Find each white blood cell.
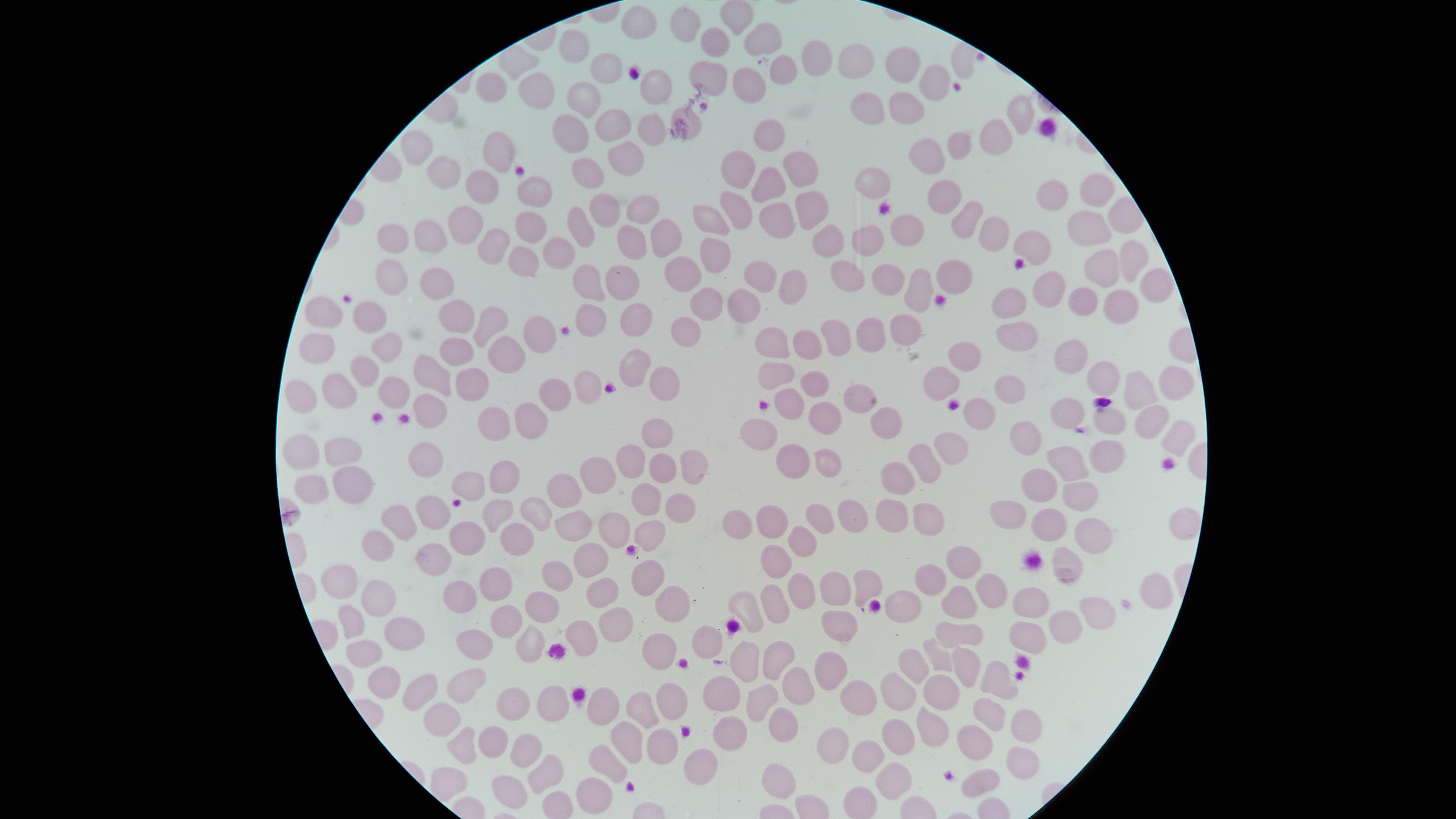

No white blood cells identified.

Approximate marker points as {x, y} in pixels. Uninfected red blood cells: {738, 19}, {640, 22}, {683, 22}, {766, 41}, {711, 42}, {572, 49}, {820, 57}, {858, 58}, {611, 63}, {786, 65}, {903, 65}, {963, 65}, {708, 76}, {647, 79}, {941, 82}, {491, 84}, {738, 86}, {542, 90}, {580, 97}, {904, 104}, {865, 111}, {1016, 112}, {688, 114}, {608, 128}, {570, 129}, {647, 129}, {996, 135}, {771, 140}, {958, 140}, {413, 147}, {498, 147}, {930, 153}, {619, 155}, {796, 162}, {738, 168}, {586, 173}, {445, 174}, {766, 179}, {868, 182}, {487, 183}, {537, 189}, {1102, 190}, {947, 191}, {1048, 197}, {802, 206}, {599, 207}, {642, 208}, {735, 209}, {1123, 212}, {709, 214}, {772, 219}, {901, 223}, {961, 227}, {461, 228}, {529, 229}, {574, 229}, {980, 230}, {1091, 231}, {667, 234}, {427, 235}, {380, 237}, {833, 239}, {868, 239}, {634, 242}, {1034, 246}, {487, 250}, {552, 253}, {703, 257}, {1130, 259}, {515, 261}, {1103, 264}, {848, 272}, {680, 273}, {392, 274}, {632, 274}, {788, 274}, {760, 275}, {436, 277}, {887, 277}, {584, 280}, {1049, 283}, {1150, 286}, {913, 288}, {711, 295}, {741, 298}, {1016, 299}, {1085, 299}, {324, 305}, {1113, 306}, {369, 311}, {634, 312}, {458, 316}, {590, 316}, {490, 330}, {903, 330}, {1018, 334}, {871, 335}, {689, 336}, {544, 337}, {843, 337}, {768, 343}, {799, 343}, {323, 345}, {387, 349}, {454, 349}, {506, 352}, {1077, 354}, {963, 357}, {639, 360}, {430, 366}, {365, 371}, {773, 374}, {665, 376}, {1104, 377}, {810, 382}, {473, 383}, {942, 383}, {581, 387}, {393, 388}, {330, 389}, {1005, 389}, {293, 392}, {1141, 392}, {1172, 392}, {559, 395}, {860, 400}, {425, 403}, {788, 404}, {978, 405}, {1070, 410}, {535, 417}, {1148, 418}, {487, 419}, {823, 420}, {888, 422}, {1108, 423}, {1034, 429}, {659, 432}, {1175, 433}, {765, 437}, {952, 441}, {302, 446}, {338, 447}, {932, 453}, {1106, 454}, {422, 458}, {688, 458}, {1075, 459}, {632, 461}, {795, 464}, {827, 464}, {658, 468}, {598, 471}, {501, 478}, {471, 480}, {898, 482}, {350, 485}, {1045, 485}, {301, 486}, {563, 492}, {643, 492}, {1076, 498}, {674, 503}, {492, 508}, {533, 509}, {431, 510}, {736, 510}, {399, 512}, {889, 512}, {924, 512}, {1010, 513}, {850, 516}, {766, 518}, {814, 518}, {568, 522}, {1181, 522}, {604, 525}, {1043, 526}, {643, 529}, {454, 536}, {1089, 536}, {507, 539}, {375, 546}, {802, 548}, {586, 555}, {421, 556}, {959, 560}, {771, 563}, {1066, 569}, {644, 573}, {340, 574}, {933, 575}, {561, 578}, {863, 579}, {609, 583}, {828, 586}, {990, 587}, {492, 589}, {803, 589}, {1159, 589}, {452, 595}, {772, 598}, {376, 599}, {744, 604}, {964, 604}, {1031, 605}, {535, 606}, {662, 606}, {1106, 612}, {907, 614}, {502, 617}, {345, 621}, {613, 624}, {1070, 624}, {838, 625}, {393, 627}, {583, 634}, {960, 634}, {1027, 635}, {468, 641}, {524, 642}, {707, 644}, {351, 645}, {653, 649}, {779, 654}, {937, 654}, {746, 656}, {966, 662}, {825, 665}, {909, 667}, {997, 677}, {476, 678}, {797, 683}, {375, 685}, {715, 685}, {416, 687}, {763, 689}, {850, 689}, {894, 691}, {939, 691}, {667, 693}, {792, 701}, {519, 705}, {551, 705}, {647, 705}, {604, 709}, {431, 711}, {929, 720}, {985, 721}, {1020, 721}, {788, 723}, {726, 727}, {832, 731}, {896, 733}, {972, 737}, {467, 738}, {631, 740}, {491, 742}, {659, 746}, {522, 750}, {697, 757}, {868, 757}, {1022, 757}, {604, 761}, {542, 771}, {889, 776}, {982, 776}, {448, 777}, {782, 779}, {584, 789}, {507, 794}. Image is 1456×819 pixels. Photographed with a smartphone camera through the microscope eyepiece. Presence: no malaria parasites detected. Single field of view. Thin blood film. The visible region is circular. Giemsa-stained preparation.